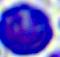

magnification = 400x
identification = leukocyte
modality = photomicrograph